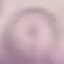 Result: no malaria parasites seen. Acquired by smartphone through the microscope eyepiece. Thin smear of blood. Cell patch, automatically extracted from a larger field of view and resized to 64 × 64 pixels. Giemsa stain.